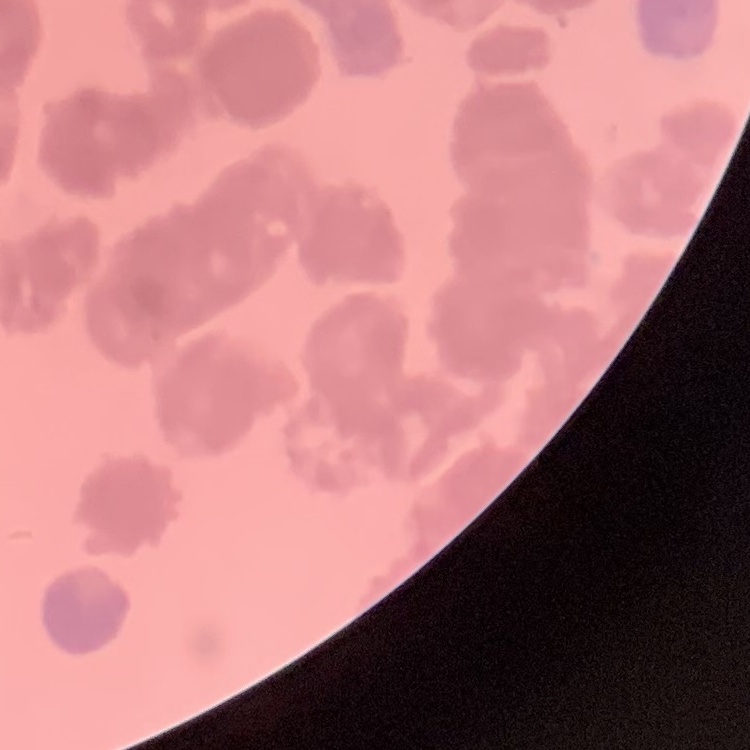
The erythrocytes show rouleaux formation. Field's or Giemsa stain. Thin peripheral smear. One tile cut from a larger photomicrograph.